Locate and identify every blood parasite.
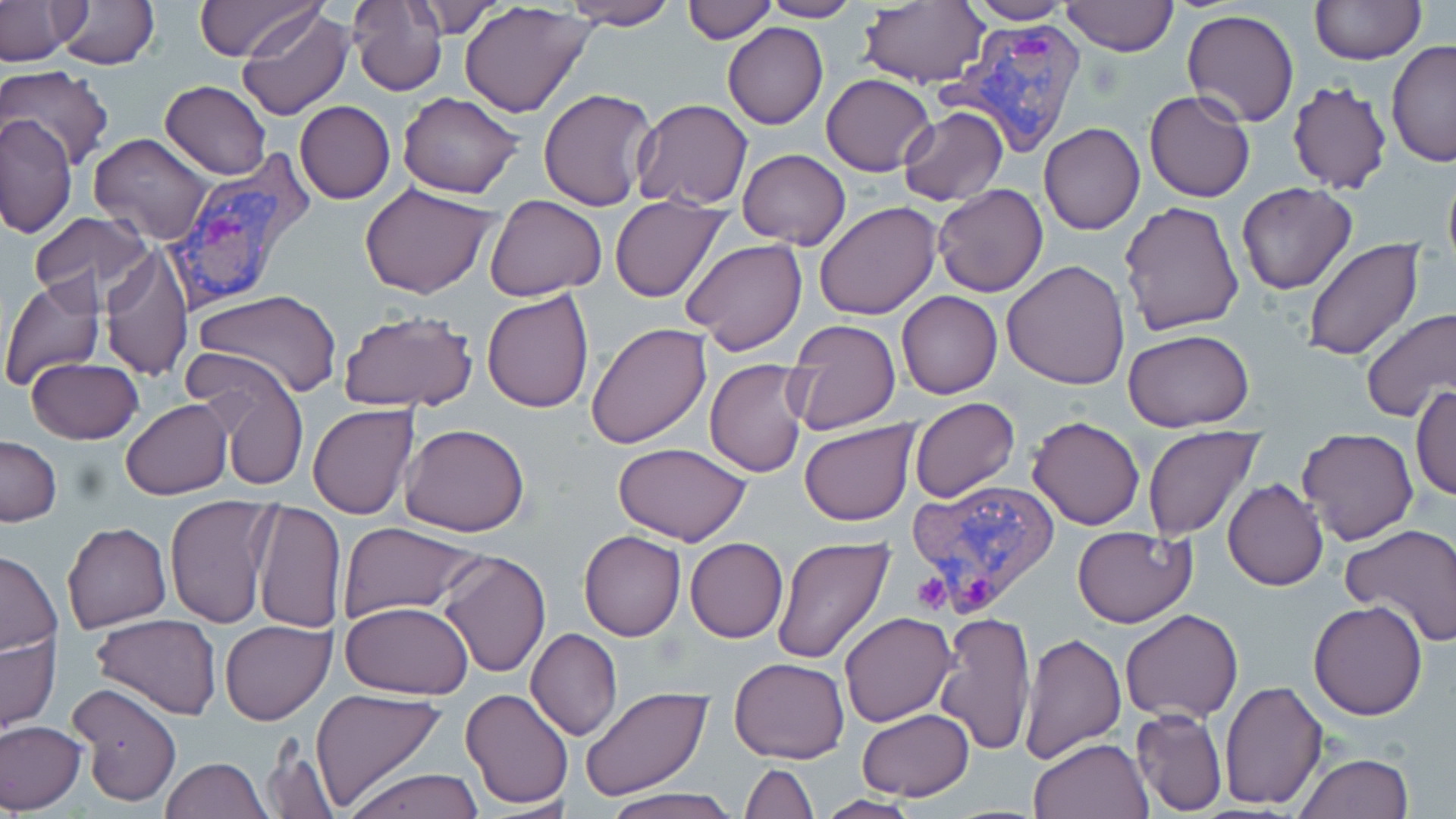

Approximate bounding boxes as (x1,y1)-(x2,y2) corner pairs in pixels.
Plasmodium vivax-infected red blood cells: (941,20)-(1083,161), (160,153)-(314,315), (910,475)-(1058,616).
No Plasmodium falciparum, Plasmodium ovale, Plasmodium malariae, Babesia divergens, or Trypanosoma brucei observed.

Uninfected red blood cell locations: (192,0)-(322,59), (758,0)-(863,22), (1310,0)-(1425,64), (52,1)-(159,70), (564,1)-(679,29), (683,1)-(775,42), (961,1)-(1080,24), (0,2)-(79,65), (347,2)-(448,95), (400,2)-(509,37), (460,2)-(596,118), (1057,2)-(1179,56), (856,3)-(988,87), (238,7)-(355,121), (1182,9)-(1300,127), (723,23)-(828,128), (1387,38)-(1456,167), (2,66)-(115,171), (822,73)-(936,177), (1286,80)-(1392,195), (159,81)-(271,179), (537,88)-(657,211), (1144,91)-(1255,204), (397,92)-(525,198), (630,99)-(754,210), (294,101)-(396,203), (897,106)-(1009,206), (1,111)-(78,238), (1039,122)-(1145,234), (88,133)-(213,245), (737,148)-(851,250), (1442,162)-(1456,281), (358,181)-(501,299), (1236,182)-(1359,295), (932,183)-(1049,297), (609,195)-(728,304), (484,196)-(606,300), (1118,201)-(1246,337), (814,202)-(941,320), (28,212)-(156,310), (681,239)-(806,354), (1301,240)-(1424,361), (101,242)-(194,383), (1002,260)-(1131,389), (1,277)-(105,391), (190,289)-(341,400), (482,289)-(596,412), (897,290)-(1003,399), (1359,307)-(1456,424), (337,309)-(479,415), (784,318)-(902,436), (585,321)-(712,449), (1122,328)-(1255,431), (186,355)-(311,492), (25,357)-(143,444), (705,358)-(810,477), (1412,386)-(1456,501), (909,397)-(1021,504), (121,399)-(232,499), (307,403)-(419,519), (1027,415)-(1145,530), (800,421)-(918,527), (399,422)-(530,536), (1142,425)-(1263,542), (1296,428)-(1419,546), (1,436)-(62,526), (612,443)-(752,546), (1223,478)-(1328,591), (165,495)-(278,630), (252,501)-(346,634), (337,521)-(482,621), (62,523)-(171,632), (1340,523)-(1456,648), (1073,525)-(1198,628), (578,530)-(685,641), (770,535)-(894,667), (684,537)-(788,643), (1,550)-(62,657), (437,550)-(551,678), (1308,601)-(1430,720), (340,602)-(476,699), (1120,608)-(1243,722), (935,610)-(1037,756), (839,612)-(956,727), (91,614)-(222,720), (218,619)-(335,724), (1,622)-(60,741), (526,629)-(622,741), (1019,633)-(1126,763), (729,657)-(850,764), (1220,678)-(1327,810), (68,681)-(182,808), (579,686)-(712,800), (459,687)-(575,810), (308,689)-(449,813), (1130,705)-(1226,815), (857,708)-(975,800), (0,720)-(86,813), (1028,737)-(1153,819), (260,742)-(339,819), (1294,752)-(1415,819), (161,756)-(270,818), (739,762)-(817,818), (344,766)-(482,819), (603,789)-(738,819), (817,794)-(921,817). Platelet locations: (910,570)-(953,616). Slide-level diagnosis: Plasmodium vivax. May-Grünwald-Giemsa stain. 1000x magnification. One field of a larger specimen. Thin blood smear. Image is 1456×819 pixels. Light microscopy.